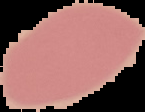

preparation = thin blood smear
image size = 145×112 pixels
image type = cell region segmented out of the field of view; surrounding area masked to black
result = no Plasmodium parasites seen